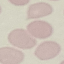
Summary:
  - Malaria status: uninfected
  - Stain: Giemsa
  - Image type: automatically extracted cell patch, resized to 64 × 64 pixels
  - Capture: smartphone camera at the microscope eyepiece
  - Preparation: thin blood smear